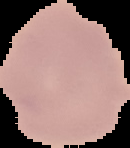
Summary:
  - Image size: 130×148 pixels
  - Image type: segmented cell region on a black background
  - Malaria status: uninfected
  - Preparation: thin blood film